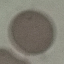
Malaria status: uninfected. Acquired by smartphone through the microscope eyepiece. Giemsa stain. Automatically extracted cell patch, resized to 64 × 64 pixels. Thin smear of blood.